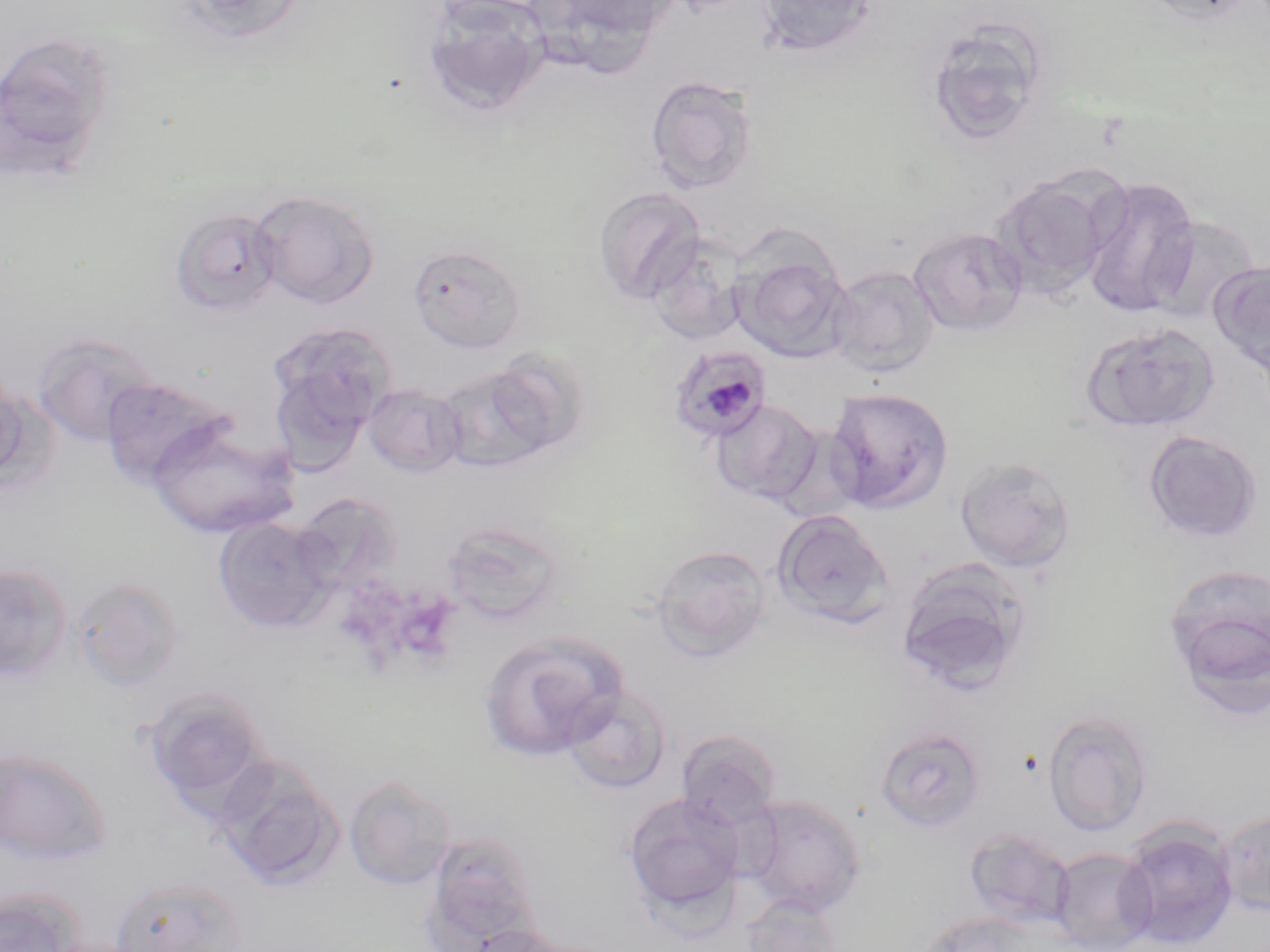
{
  "slide_level_diagnosis": "Plasmodium malariae",
  "field_of_view": "single",
  "stain": "May-Grünwald-Giemsa",
  "image_size": "1270×952 pixels",
  "uninfected_red_blood_cell_locations": "approximate bounding boxes as (x1,y1)-(x2,y2) corner pairs in pixels: (171,0)-(309,45), (421,0)-(551,116), (533,0)-(680,61), (754,0)-(880,60), (1136,0)-(1259,25), (924,23)-(1046,146), (0,31)-(117,177), (644,75)-(758,192), (990,173)-(1119,300), (1079,176)-(1201,317), (593,187)-(706,304), (249,189)-(380,309), (170,208)-(282,317), (1145,216)-(1263,326), (909,225)-(1029,337), (645,234)-(748,346), (408,244)-(526,353), (732,250)-(853,362), (1207,262)-(1270,368), (827,266)-(941,377), (1080,322)-(1220,433), (267,323)-(390,465), (31,331)-(161,448), (483,349)-(590,458), (435,363)-(559,474), (0,367)-(34,484), (100,376)-(232,489), (363,383)-(467,477), (825,388)-(953,513), (711,398)-(824,507), (146,418)-(298,539), (1143,430)-(1264,544), (954,456)-(1077,573), (291,492)-(405,593), (771,509)-(895,628), (212,517)-(335,632), (439,518)-(569,626), (650,544)-(772,662), (894,559)-(1034,694), (0,564)-(72,683), (1162,565)-(1270,717), (71,576)-(184,693), (478,631)-(629,761), (562,686)-(672,794), (142,688)-(272,816), (1042,710)-(1154,835), (874,727)-(986,834), (676,730)-(782,830), (0,748)-(111,865), (212,756)-(344,889), (343,775)-(458,890), (622,793)-(747,921), (738,794)-(868,918), (1218,808)-(1270,917), (1117,821)-(1239,949), (964,828)-(1076,930), (422,829)-(541,947), (1051,847)-(1157,951), (108,875)-(248,952), (0,889)-(83,952), (740,894)-(844,952), (920,911)-(1039,952), (467,924)-(571,952)",
  "modality": "optical microscopy",
  "plasmodium_malariae_infected_red_blood_cell_locations": "approximate bounding boxes as (x1,y1)-(x2,y2) corner pairs in pixels: (666,343)-(772,442)",
  "magnification": "1000x",
  "preparation": "thin blood smear"
}